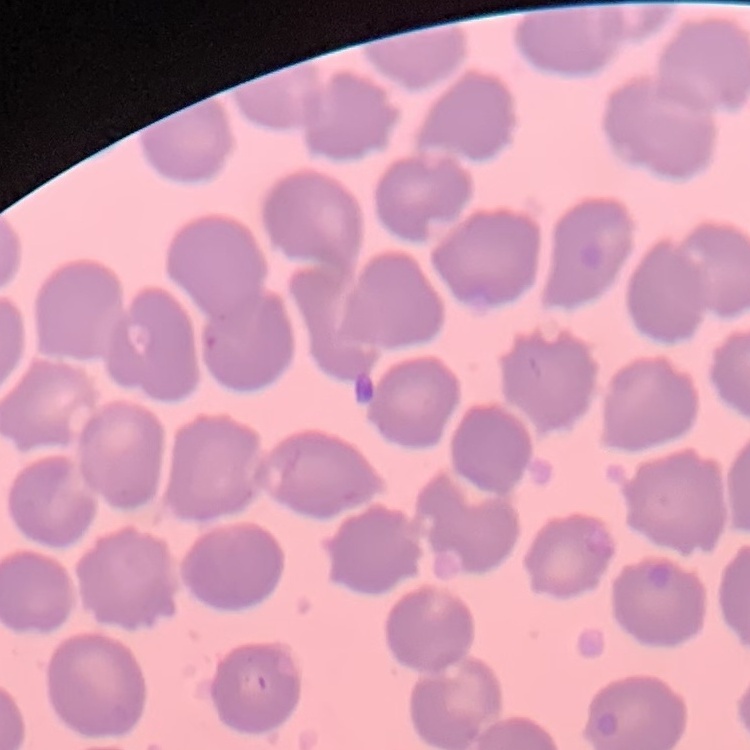

{
  "erythrocyte_morphology": "no rouleaux formation",
  "stain": "Field's or Giemsa",
  "image_type": "one tile cut from a larger photomicrograph",
  "preparation": "thin blood film"
}